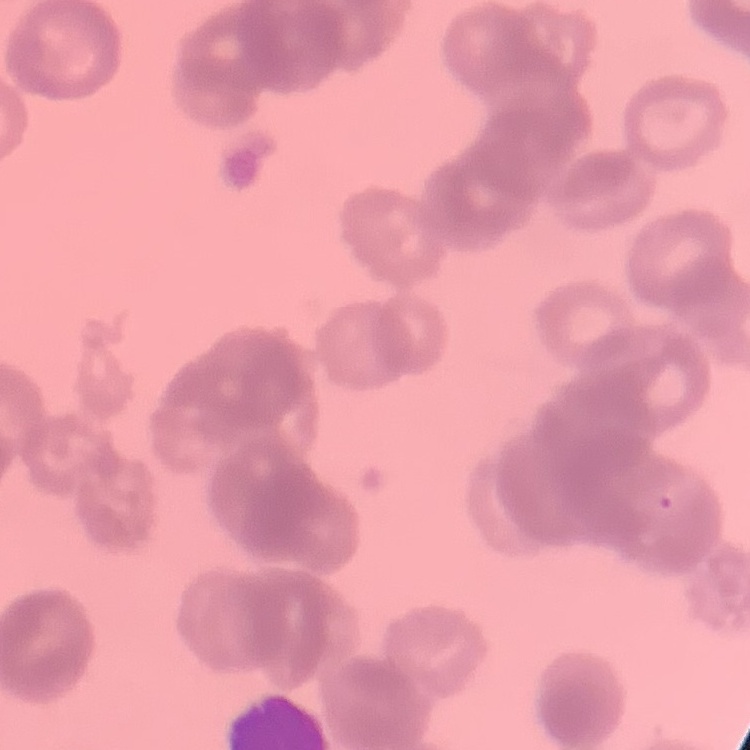
The erythrocytes exhibit rouleaux formation. Stained with either Field's or Giemsa. Thin blood film. One tile cut from a larger photomicrograph.